Identify the blood parasite species.
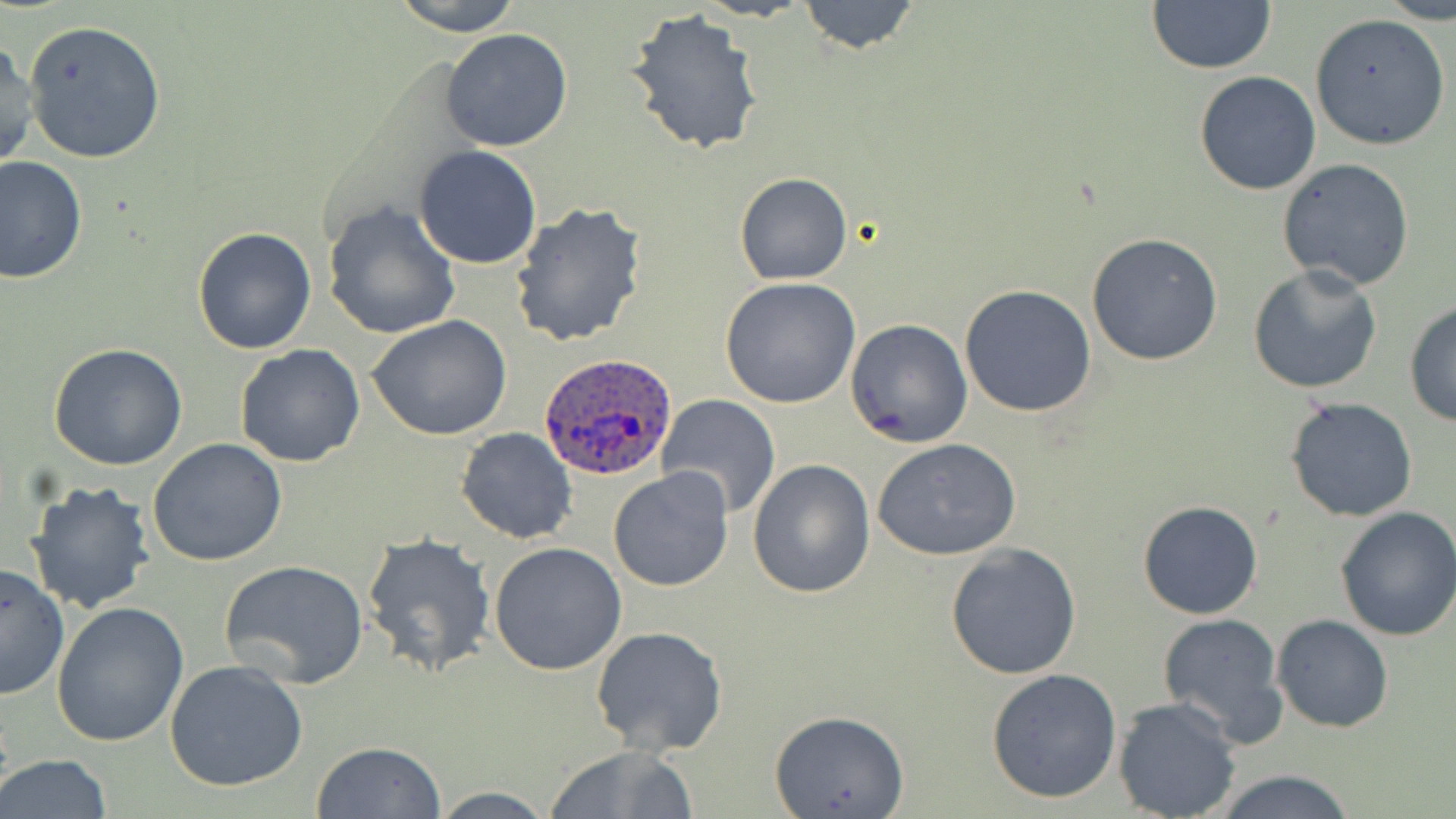
Plasmodium ovale.

Approximate bounding boxes as [x1, y1, x2, y2] in pixels. Plasmodium ovale-infected red blood cell locations: [541, 355, 677, 481]. Uninfected red blood cell locations: [389, 0, 528, 35], [796, 0, 921, 55], [1145, 1, 1276, 74], [624, 9, 764, 155], [1310, 14, 1450, 150], [22, 20, 166, 164], [440, 29, 573, 152], [434, 33, 558, 272], [0, 37, 39, 172], [1194, 71, 1321, 196], [414, 145, 543, 269], [1, 156, 87, 283], [1276, 158, 1416, 290], [735, 172, 853, 285], [322, 200, 461, 340], [510, 201, 646, 347], [191, 226, 318, 355], [1085, 233, 1224, 366], [1245, 263, 1386, 396], [719, 278, 860, 409], [959, 285, 1098, 416], [1403, 299, 1456, 426], [366, 314, 514, 441], [845, 319, 973, 448], [47, 342, 190, 469], [235, 343, 367, 467], [658, 395, 781, 519], [1284, 397, 1420, 522], [456, 427, 579, 545], [147, 438, 288, 566], [873, 438, 1022, 561], [747, 459, 875, 599], [608, 466, 734, 592], [25, 480, 158, 615], [1137, 498, 1265, 620], [1335, 506, 1456, 643], [361, 531, 496, 678], [488, 541, 627, 675], [945, 544, 1081, 681], [219, 559, 369, 686], [1, 565, 71, 701], [52, 600, 189, 748], [1157, 612, 1289, 743], [1272, 614, 1395, 732], [590, 627, 730, 757], [165, 660, 309, 793], [986, 667, 1122, 803], [1113, 697, 1241, 818], [769, 710, 911, 818], [312, 742, 445, 819], [541, 743, 701, 819], [1, 754, 113, 819], [1211, 771, 1361, 818], [427, 785, 559, 818]. May-Grünwald-Giemsa-stained preparation. Light microscopy. One field of a larger specimen. Captured at 1000x magnification. Thin blood smear. Image is 1456×819 pixels.